Look for Plasmodium parasites.
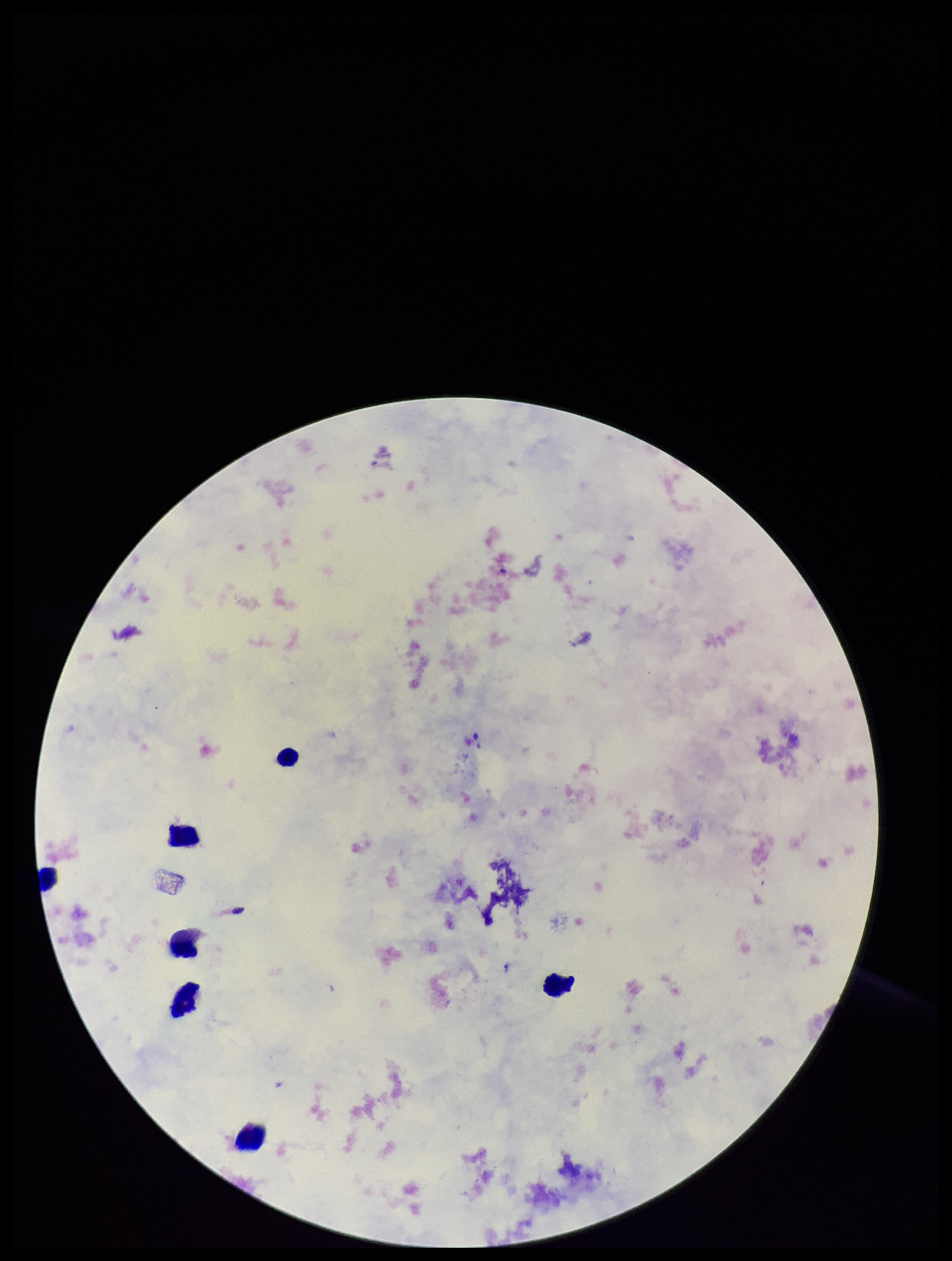
None identified.

Smartphone photograph taken through the eyepiece of a microscope. Patient malaria status: negative. One field from this slide. Leukocyte count: 6. Giemsa stain. Parasite count: 0. Preparation: thick. Image is 952×1261 pixels.